Locate every leukocyte (white blood cell).
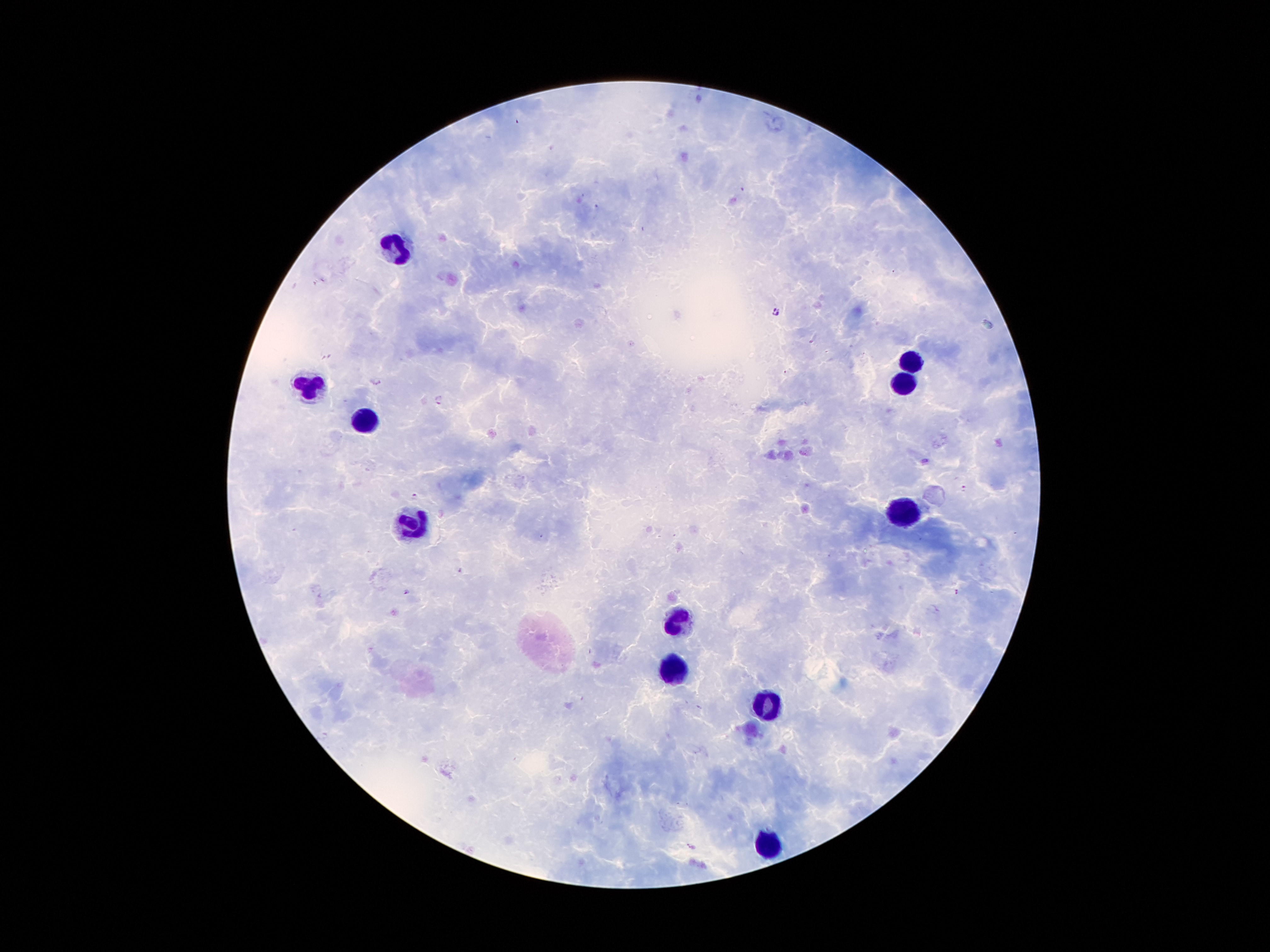

Approximate centers as {x, y} in pixels.
Leukocytes: {398, 251}, {915, 359}, {904, 383}, {310, 387}, {362, 422}, {902, 518}, {413, 527}, {676, 624}, {678, 671}, {764, 701}, {769, 844}.

Summary:
  - Plasmodium parasite locations: {775, 312}, {377, 382}, {440, 400}, {964, 488}, {415, 497}, {461, 571}, {407, 591}, {957, 592}, {692, 847}
  - Magnification: 100x
  - Capture: smartphone through the microscope eyepiece
  - Preparation: thick blood film
  - Patient malaria status: positive for Plasmodium falciparum
  - Image size: 1270×952 pixels
  - Field of view: one from this slide
  - Stain: Giemsa